Point out leukocytes.
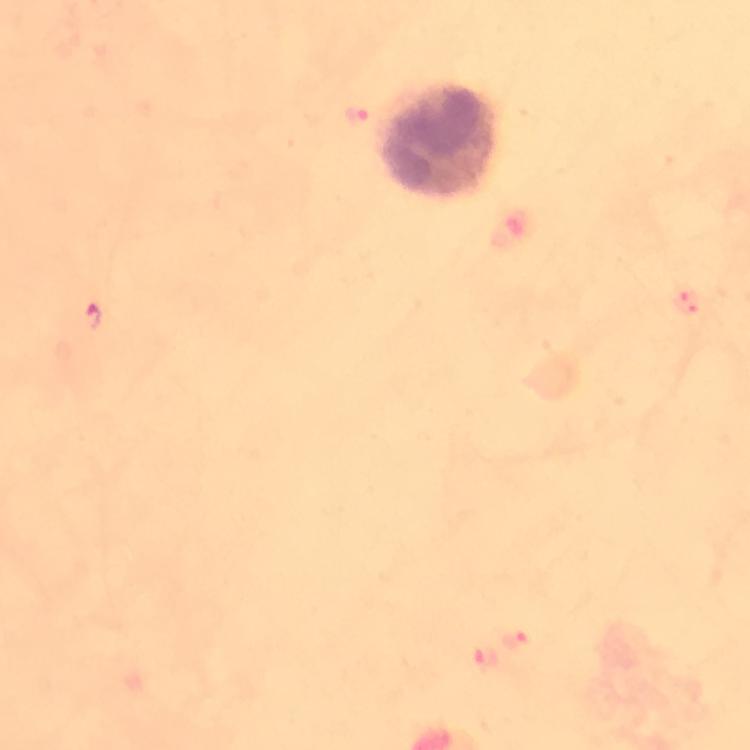

Approximate centers as [x, y] in pixels.
Leukocytes: [443, 140].

Summary:
  - Plasmodium parasite locations: [357, 115], [687, 302], [91, 318], [512, 639], [484, 656]
  - Immersion oil: used
  - Magnification: 100x
  - Context: from a diagnostic examination for malaria
  - Stain: Giemsa
  - Image size: 750×750 pixels
  - Cropped from: a single field of view
  - Preparation: thick blood film
  - Capture: smartphone photograph through a microscope